Locate every Plasmodium ovale-infected red blood cell.
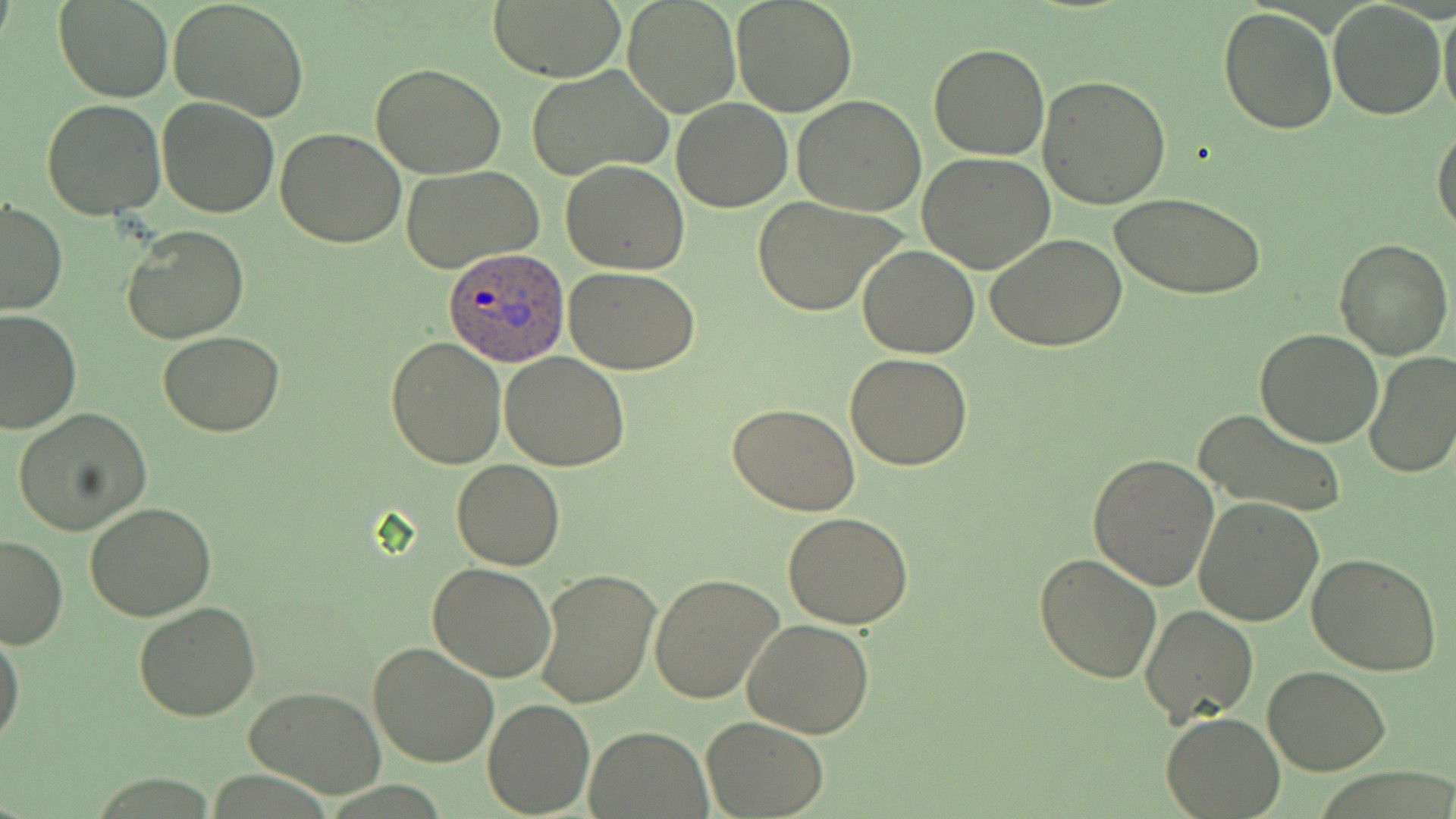
Approximate bounding boxes as (x1, y1, x2, y2) in pixels.
Plasmodium ovale-infected red blood cells: (442, 249, 570, 367).

{
  "slide_level_diagnosis": "Plasmodium ovale",
  "image_size": "1456×819 pixels",
  "modality": "light microscopy",
  "preparation": "thin blood film",
  "stain": "May-Grünwald-Giemsa",
  "uninfected_red_blood_cell_locations": "approximate bounding boxes as (x1, y1, x2, y2) in pixels: (56, 0, 173, 103), (168, 0, 311, 122), (489, 0, 624, 80), (731, 0, 858, 117), (1329, 1, 1446, 119), (1438, 1, 1456, 121), (623, 2, 738, 116), (1219, 5, 1338, 134), (929, 43, 1049, 160), (371, 62, 506, 178), (525, 66, 671, 181), (1040, 75, 1172, 210), (791, 95, 927, 216), (156, 97, 280, 219), (670, 97, 793, 211), (42, 100, 167, 220), (276, 126, 405, 247), (1432, 126, 1456, 238), (917, 153, 1057, 275), (561, 160, 689, 275), (402, 166, 543, 275), (1111, 192, 1266, 300), (751, 195, 907, 316), (1, 198, 67, 314), (123, 225, 249, 343), (986, 233, 1127, 351), (1333, 236, 1454, 360), (859, 246, 980, 358), (565, 268, 700, 375), (0, 310, 80, 434), (1255, 327, 1384, 446), (158, 331, 286, 436), (386, 337, 506, 468), (499, 351, 630, 471), (1363, 352, 1456, 480), (844, 353, 974, 471), (728, 402, 861, 515), (13, 408, 151, 534), (1194, 409, 1348, 520), (1087, 453, 1220, 592), (451, 459, 564, 570), (1194, 496, 1325, 627), (85, 502, 217, 622), (784, 511, 913, 628), (0, 533, 68, 650), (1035, 553, 1163, 684), (1307, 553, 1442, 677), (428, 562, 557, 681), (533, 565, 661, 709), (649, 573, 785, 703), (133, 601, 260, 720), (1139, 604, 1259, 727), (742, 616, 875, 738), (0, 626, 23, 747), (367, 641, 499, 770), (1264, 665, 1390, 776), (244, 686, 387, 798), (483, 698, 595, 817), (1161, 713, 1286, 818), (702, 716, 828, 817), (586, 726, 711, 817)",
  "field_of_view": "one of a larger specimen",
  "magnification": "1000x"
}